Locate and identify every blood parasite.
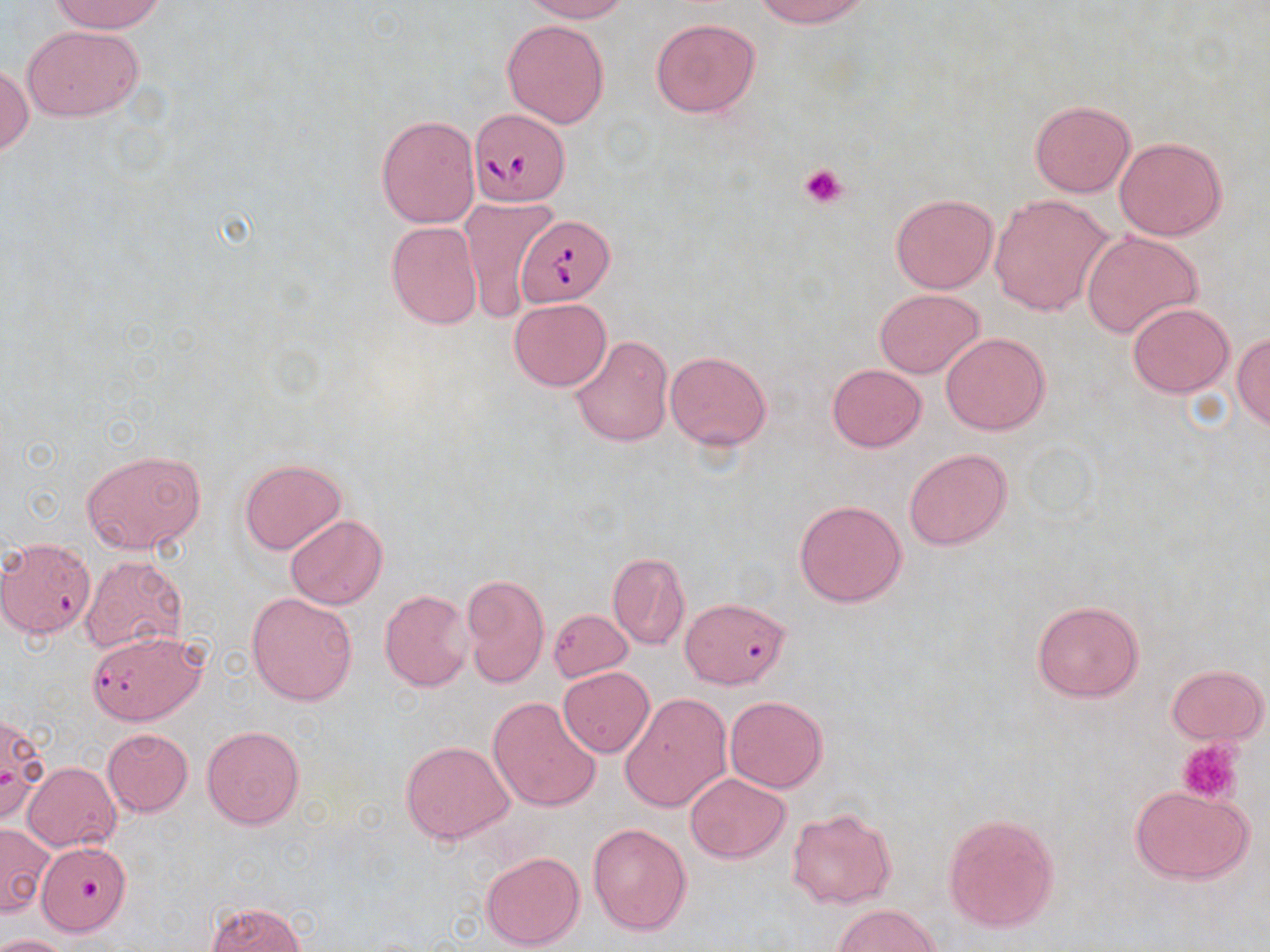
Approximate bounding boxes as [x1, y1, x2, y2] in pixels.
Babesia divergens-infected red blood cells: [468, 108, 570, 207], [515, 216, 614, 306], [87, 630, 205, 725].
No Plasmodium falciparum, Plasmodium ovale, Plasmodium malariae, Plasmodium vivax, or Trypanosoma brucei observed.

Summary:
  - Uninfected red blood cell locations: [50, 0, 164, 34], [522, 0, 628, 22], [753, 0, 871, 27], [650, 17, 760, 118], [503, 19, 610, 127], [24, 24, 144, 121], [0, 63, 32, 158], [1029, 100, 1135, 196], [376, 115, 480, 227], [1114, 136, 1227, 240], [890, 193, 997, 293], [989, 196, 1114, 315], [459, 198, 556, 322], [386, 221, 483, 329], [1081, 230, 1202, 339], [874, 289, 985, 378], [510, 298, 610, 391], [1127, 302, 1233, 397], [940, 332, 1050, 435], [1232, 332, 1270, 430], [570, 334, 675, 447], [665, 350, 772, 450], [826, 364, 927, 452], [904, 447, 1013, 550], [81, 449, 207, 554], [240, 458, 347, 554], [794, 499, 907, 606], [286, 515, 387, 610], [2, 540, 90, 642], [79, 553, 190, 654], [607, 553, 689, 650], [461, 574, 549, 688], [380, 590, 472, 690], [247, 592, 358, 706], [1031, 599, 1144, 702], [678, 601, 793, 693], [549, 609, 632, 681], [1166, 664, 1268, 744], [558, 666, 654, 756], [620, 692, 731, 812], [489, 696, 602, 814], [725, 696, 827, 793], [0, 712, 47, 823], [202, 726, 304, 830], [103, 728, 193, 817], [401, 741, 514, 844], [21, 762, 121, 851], [685, 773, 790, 863], [1130, 786, 1255, 884], [787, 807, 897, 908], [943, 812, 1060, 933], [588, 822, 692, 937], [1, 823, 54, 917], [38, 846, 135, 938], [482, 851, 585, 951], [206, 902, 306, 952], [833, 904, 939, 951], [0, 934, 72, 952]
  - Platelet locations: [799, 163, 847, 209], [1177, 737, 1244, 806]
  - Slide-level diagnosis: Babesia divergens
  - Preparation: thin blood film
  - Image size: 1270×952 pixels
  - Stain: May-Grünwald-Giemsa
  - Modality: light microscopy
  - Magnification: 1000x
  - Field of view: one of a larger specimen